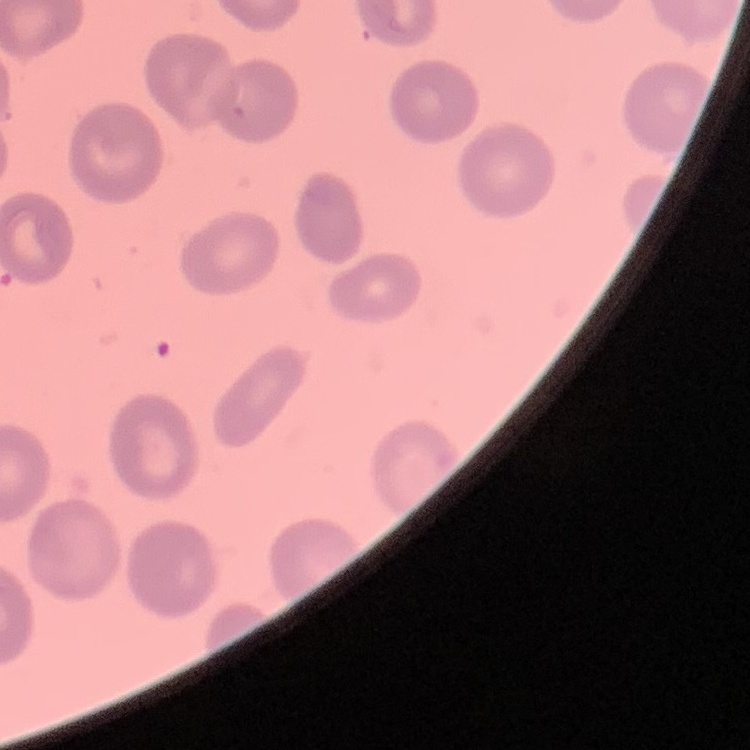

erythrocyte_morphology: no rouleaux formation
stain: Field's or Giemsa
image_type: square crop of a larger photomicrograph
preparation: thin blood film